Name the cell type shown.
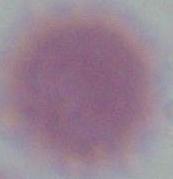
This is an erythrocyte.

magnification = 1000x
modality = photomicrograph